Report the malaria status of this cell.
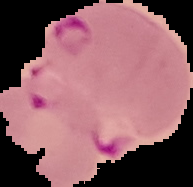
It is parasitized.

Summary:
  - Preparation: thin blood film
  - Image type: segmented cell region with the area outside set to black
  - Image size: 193×187 pixels